Locate every Plasmodium parasite.
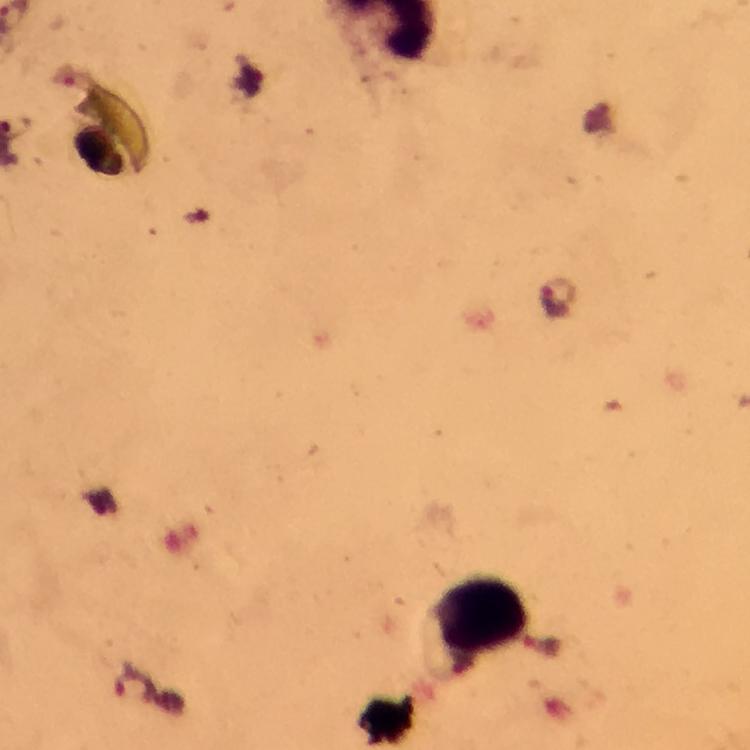

Approximate centers as {x, y} in pixels.
Plasmodium parasites: {557, 296}, {134, 686}.

image_size: 750×750 pixels
magnification: 100x
stain: Giemsa
context: from a malaria diagnostic workup
leukocyte_locations: 'approximate centers as {x, y} in pixels: {480, 619}'
preparation: thick blood film
cropped_from: a single field of view
immersion_oil: applied
capture: smartphone photograph through a microscope